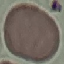

result = no malaria parasites detected
stain = Giemsa
preparation = thin blood film
capture = smartphone camera at the microscope eyepiece
image type = automatically extracted cell patch, resized to 64 × 64 pixels